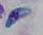
magnification = 1000x
modality = micrograph
identification = Toxoplasma gondii